Assess the morphology of the red blood cells.
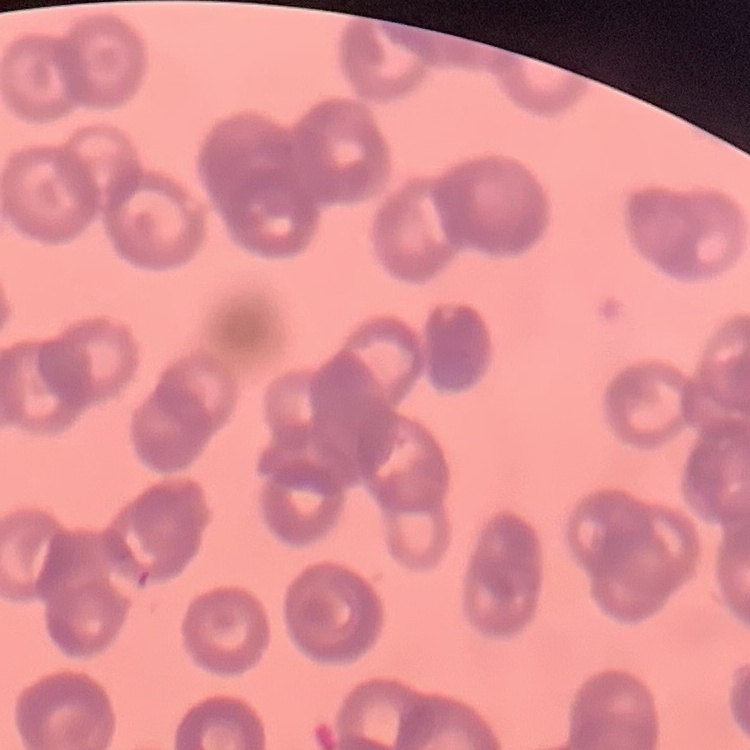
They show rouleaux formation.

{
  "stain": "Field's or Giemsa",
  "image_type": "square crop of a larger photomicrograph",
  "preparation": "thin peripheral smear"
}